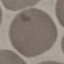

Result: no malaria parasites detected. Giemsa stain. Thin smear of blood. Cell patch, automatically extracted from a larger field of view and resized to 64 × 64 pixels. Acquired by smartphone through the microscope eyepiece.